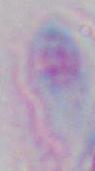

identification = Toxoplasma gondii
modality = micrograph
magnification = 1000x